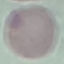

result = no malaria parasites seen
image type = automatically extracted cell patch, resized to 64 × 64 pixels
stain = Giemsa
preparation = thin smear
capture = smartphone camera at the microscope eyepiece